Comment on the morphology of the erythrocytes.
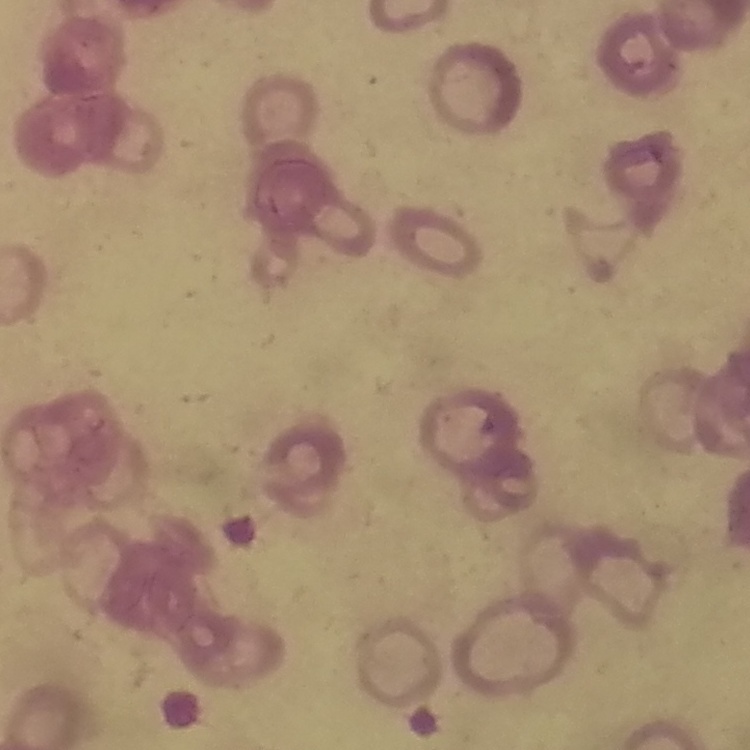

Rouleaux formation.

Summary:
  - Stain: Field's or Giemsa
  - Preparation: thin peripheral smear
  - Image type: one tile cut from a larger photomicrograph